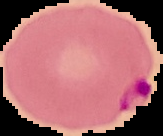
preparation = thin blood smear
result = Plasmodium parasites detected
image size = 163×136 pixels
image type = segmented cell region with the area outside set to black